Give the position of every Plasmodium parasite and every leukocyte.
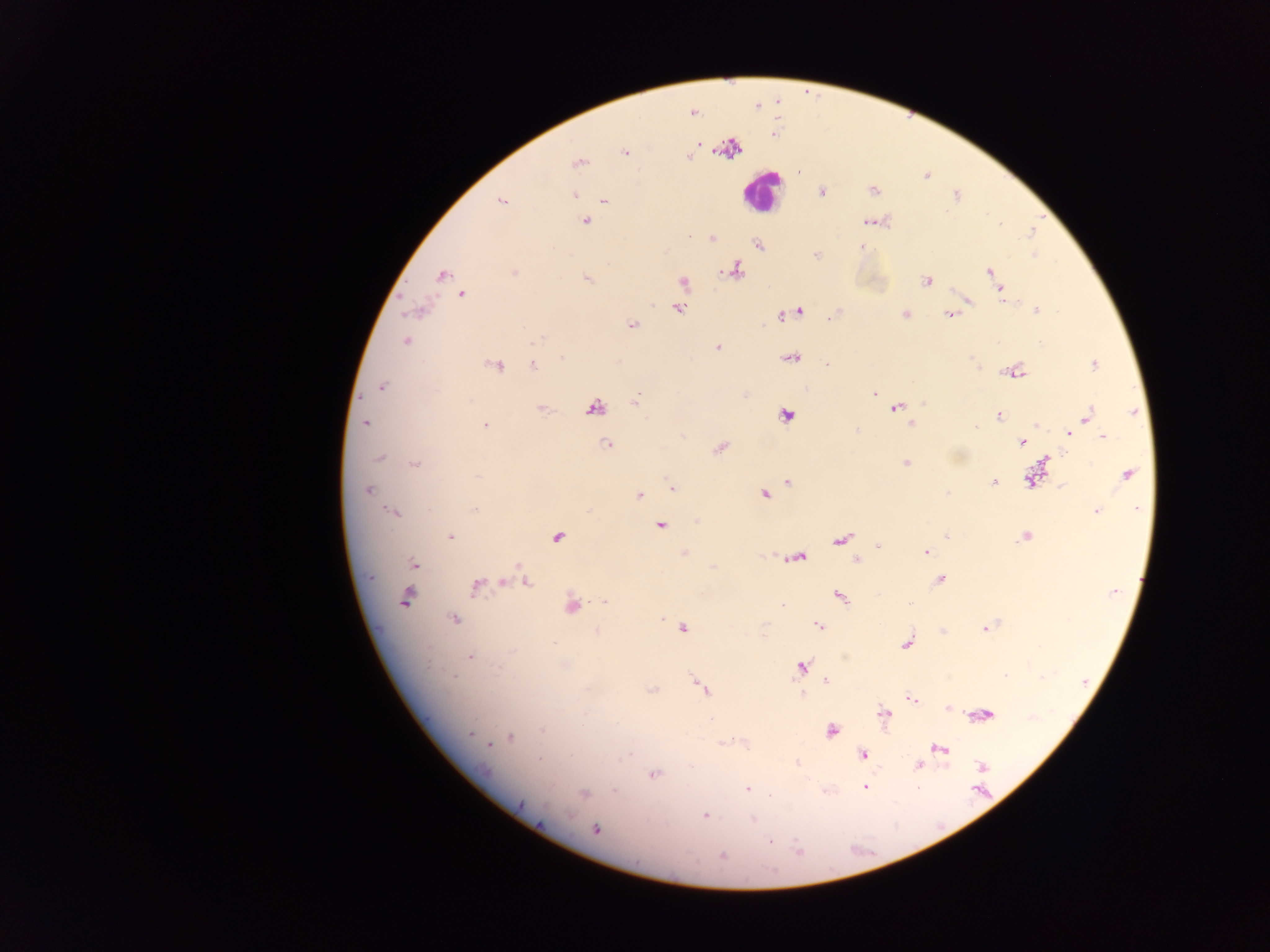
Approximate centers as [x, y] in pixels.
Plasmodium parasites: [694, 113], [625, 151], [688, 157], [578, 163], [822, 192], [575, 195], [501, 200], [604, 201], [585, 222], [869, 222], [1001, 224], [713, 238], [759, 245], [860, 247], [816, 255], [1034, 255], [734, 270], [990, 271], [514, 272], [442, 275], [586, 278], [926, 280], [683, 282], [1000, 289], [461, 294], [967, 301], [678, 309], [1036, 310], [419, 311], [799, 311], [782, 315], [905, 315], [950, 315], [631, 325], [537, 339], [405, 341], [717, 347], [791, 357], [562, 358], [972, 359], [532, 364], [827, 364], [1094, 365], [494, 366], [1015, 372], [382, 388], [874, 393], [635, 399], [923, 403], [593, 408], [896, 408], [542, 410], [1133, 411], [786, 416], [998, 416], [1088, 416], [365, 422], [911, 424], [1037, 425], [485, 426], [976, 428], [1075, 429], [857, 430], [1068, 433], [682, 435], [1103, 436], [1021, 443], [606, 445], [719, 448], [379, 458], [1045, 460], [415, 463], [906, 463], [1128, 474], [478, 477], [1031, 480], [789, 482], [993, 482], [1062, 486], [672, 489], [367, 491], [947, 493], [639, 495], [764, 495], [1137, 508], [475, 509], [1096, 511], [393, 513], [696, 521], [661, 525], [946, 536], [450, 537], [1025, 537], [557, 538], [840, 540], [878, 545], [925, 552], [684, 553], [796, 558], [856, 560], [413, 564], [519, 565], [939, 579], [503, 582], [528, 583], [476, 585], [1113, 592], [839, 596], [405, 598], [605, 602], [909, 603], [781, 604], [571, 605], [661, 619], [454, 620], [819, 626], [682, 629], [985, 629], [598, 630], [554, 643], [907, 643], [511, 651], [470, 657], [801, 667], [1005, 675], [453, 676], [1043, 676], [825, 681], [701, 688], [652, 690], [802, 694], [912, 699], [948, 709], [884, 714], [985, 715], [542, 730], [831, 731], [471, 734], [510, 738], [728, 741], [488, 744], [940, 749], [863, 755], [627, 756], [539, 759], [796, 762], [918, 766], [982, 767], [655, 774], [865, 787], [748, 788], [615, 791], [584, 793], [771, 795], [705, 815], [753, 818], [595, 829], [770, 842], [799, 849], [723, 857].
Leukocytes: [761, 191].

Thick blood smear. Image is 1270×952 pixels. Single field of view. Photographed through a microscope with a mobile-phone camera. Collected in Ghana.